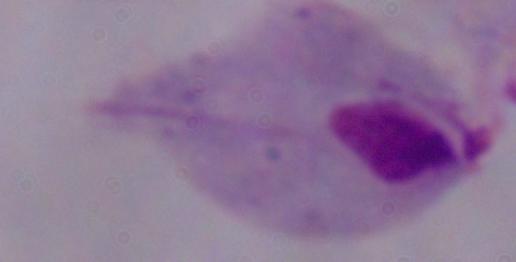
magnification: 1000x
identification: trichomonad
modality: micrograph